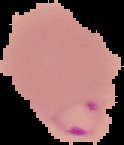

image size = 124×145 pixels
image type = segmented cell region with the area outside set to black
preparation = thin blood film
result = malaria parasites detected